Describe the morphology of the erythrocytes.
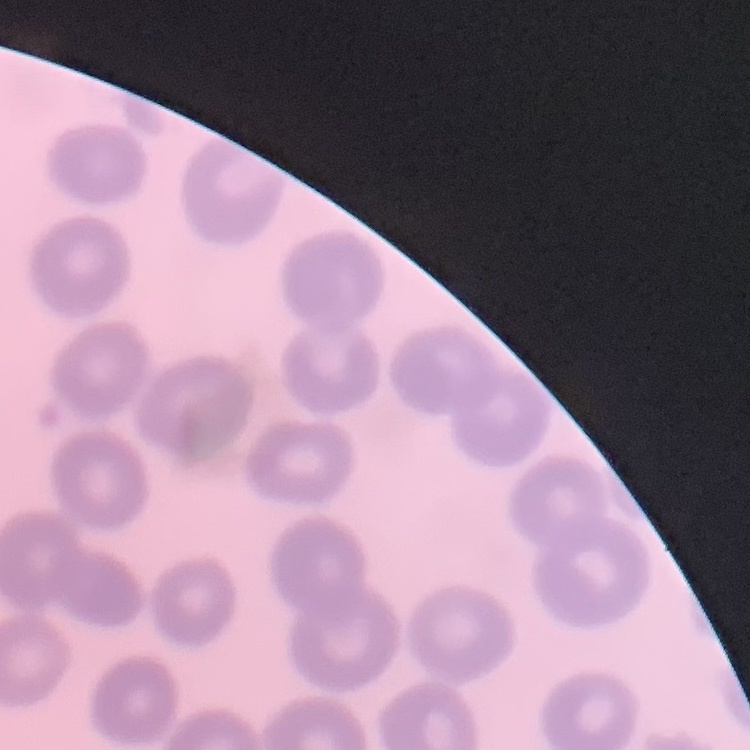
They show no rouleaux formation.

Field's or Giemsa stain. Thin blood smear. One tile cut from a larger photomicrograph.